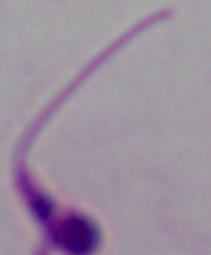

A Leishmania parasite is seen. Photomicrograph. 1000x magnification.